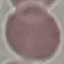
Summary:
  - Result: negative for malaria parasites
  - Preparation: thin blood film
  - Stain: Giemsa
  - Capture: smartphone camera at the microscope eyepiece
  - Image type: automatically extracted cell patch, resized to 64 × 64 pixels